Classify this cell by malaria status.
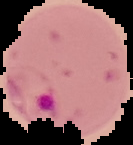

Parasitized.

Summary:
  - Image size: 133×145 pixels
  - Image type: segmented cell region on a black background
  - Preparation: thin blood film